Identify the parasite.
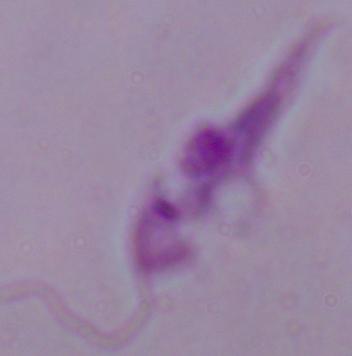

Leishmania.

modality = photomicrograph
magnification = 1000x